Classify this cell by malaria status.
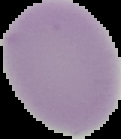
It is uninfected.

image type = cell region segmented out of the field of view; surrounding area masked to black
image size = 121×139 pixels
preparation = thin blood film